Assess this cell for malaria.
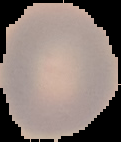

Uninfected.

From a thin blood smear. The area outside the segmented cell region is set to black. Image is 121×142 pixels.